Classify this cell by malaria status.
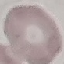

It is uninfected.

Thin blood film. Cell patch, automatically extracted from a larger field of view and resized to 64 × 64 pixels. Giemsa-stained preparation. Acquired by smartphone through the microscope eyepiece.